Identify the parasite.
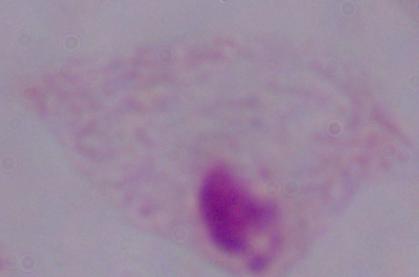
This is a trichomonad.

Summary:
  - Modality: micrograph
  - Magnification: 1000x